Classify the preparation.
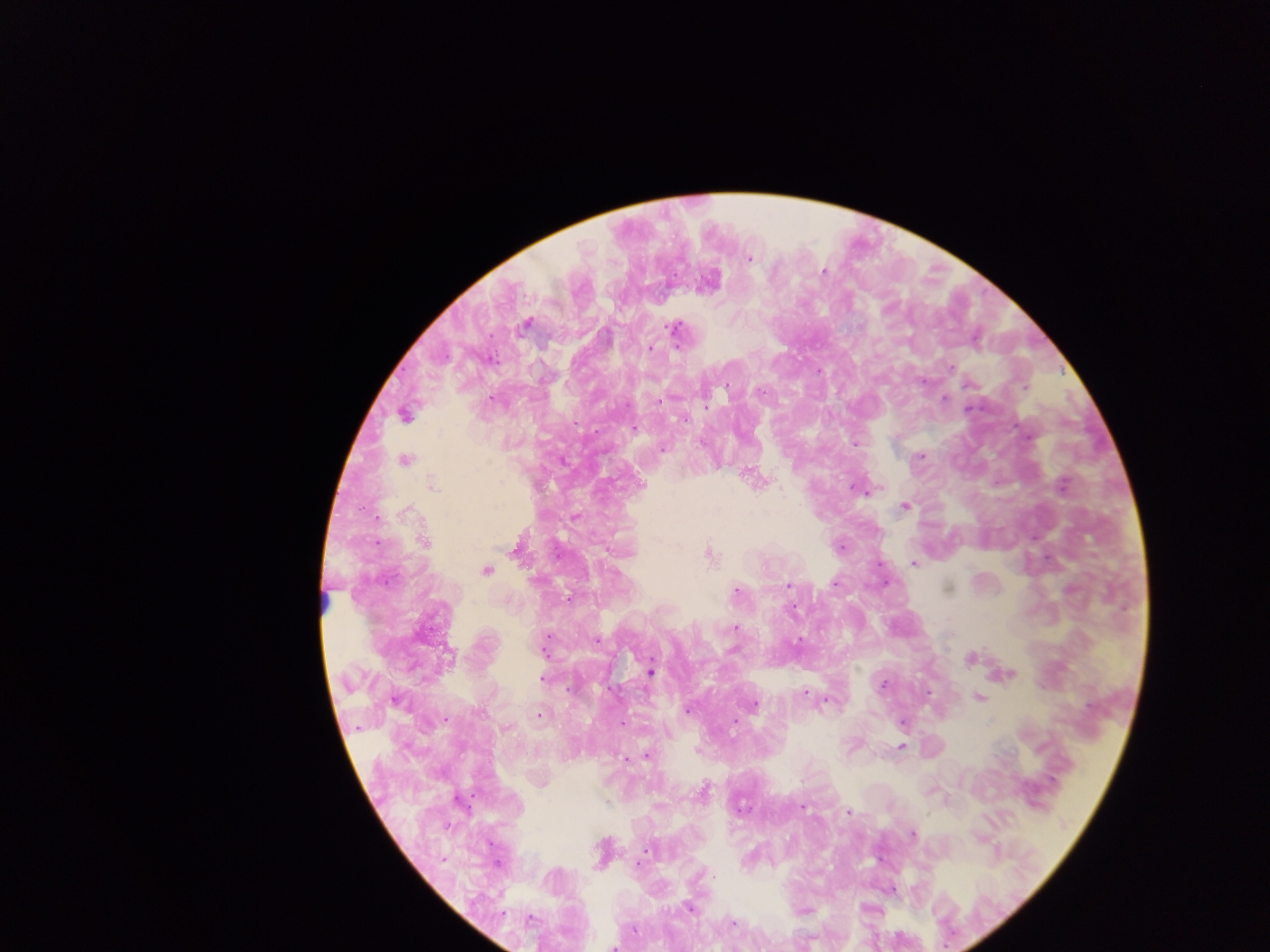
This is a thick smear.

capture = mobile-phone photograph through a microscope
country = Ghana
Plasmodium parasite locations = approximate centers as [x, y] in pixels: [748, 258], [823, 273], [707, 280], [525, 324], [675, 329], [650, 347], [950, 368], [969, 384], [1024, 387], [944, 399], [660, 400], [704, 407], [404, 414], [633, 427], [855, 444], [662, 448], [920, 455], [403, 460], [561, 460], [750, 475], [432, 484], [857, 487], [865, 489], [905, 506], [574, 517], [423, 541], [842, 547], [708, 555], [914, 563], [486, 570], [835, 582], [885, 582], [789, 584], [736, 591], [568, 597], [735, 628], [546, 643], [970, 658], [651, 672], [1004, 674], [542, 677], [883, 684], [803, 693], [978, 697], [395, 700], [826, 701], [753, 704], [687, 709], [538, 715], [733, 720], [622, 724], [901, 747], [647, 755], [625, 758], [703, 791], [930, 791], [802, 806], [848, 812], [912, 834], [601, 852], [688, 908], [803, 911], [734, 923], [612, 946], [734, 946]
image size = 1270×952 pixels
field of view = single